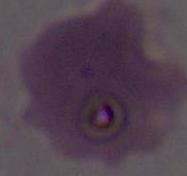

Micrograph. An erythrocyte is shown. 1000x magnification.